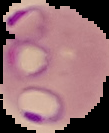
From a thin blood film. Image is 109×133 pixels. Segmented cell region on a black background. Malaria status: parasitized.